Identify the blood parasite species.
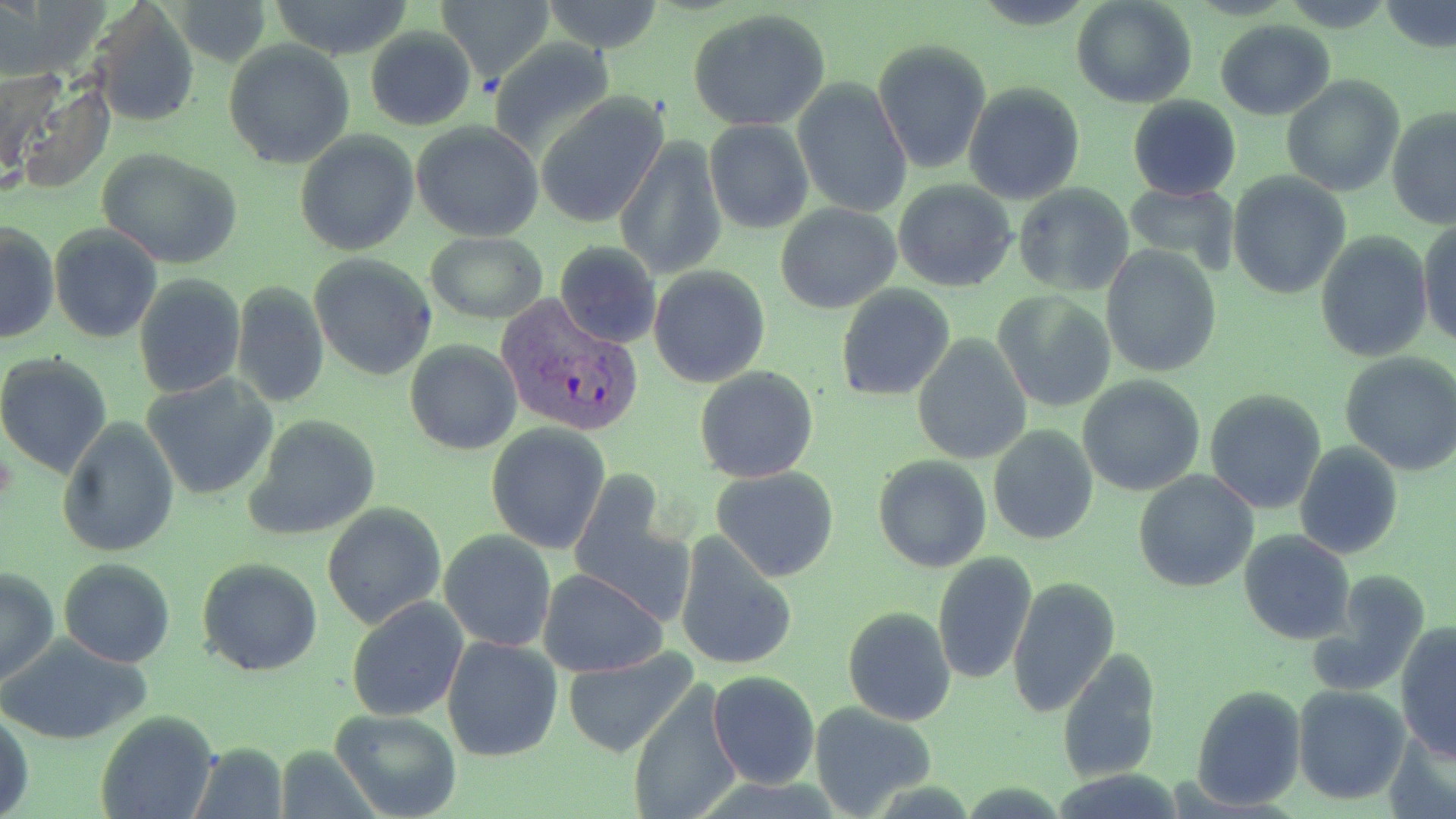
Plasmodium vivax.

Approximate bounding boxes as (x1, y1, x2, y2) in pixels. Plasmodium vivax-infected red blood cell locations: (495, 294, 646, 439). Uninfected red blood cell locations: (173, 0, 271, 67), (268, 0, 417, 61), (435, 0, 553, 82), (539, 0, 668, 53), (1072, 0, 1198, 109), (1381, 2, 1456, 53), (88, 3, 201, 128), (687, 10, 832, 132), (1215, 19, 1335, 119), (364, 28, 477, 131), (488, 38, 617, 158), (873, 40, 993, 176), (223, 41, 354, 170), (4, 69, 114, 195), (1280, 75, 1404, 198), (792, 78, 912, 218), (962, 82, 1085, 206), (537, 92, 670, 230), (1127, 94, 1242, 201), (1387, 106, 1456, 229), (704, 120, 815, 235), (411, 121, 545, 242), (294, 129, 420, 258), (615, 137, 729, 280), (96, 148, 243, 269), (1227, 173, 1350, 300), (892, 179, 1017, 293), (1013, 182, 1136, 297), (1125, 182, 1238, 273), (775, 203, 901, 315), (1417, 218, 1456, 350), (1, 219, 59, 346), (49, 224, 163, 345), (424, 232, 548, 323), (1315, 232, 1432, 363), (552, 240, 662, 350), (1099, 245, 1221, 378), (310, 254, 437, 379), (647, 266, 772, 388), (133, 274, 246, 398), (231, 282, 330, 407), (835, 284, 956, 402), (991, 291, 1116, 415), (912, 334, 1032, 465), (403, 340, 522, 456), (1339, 351, 1456, 477), (0, 354, 114, 479), (695, 366, 820, 483), (1078, 374, 1205, 497), (142, 375, 278, 501), (1204, 389, 1326, 514), (244, 415, 381, 542), (58, 419, 179, 557), (486, 424, 611, 554), (987, 425, 1098, 546), (873, 440, 1101, 557), (1293, 442, 1403, 560), (873, 455, 993, 573), (710, 466, 840, 582), (1133, 470, 1258, 592), (570, 473, 685, 610), (322, 503, 448, 630), (438, 528, 557, 653), (1238, 530, 1354, 644), (673, 533, 800, 673), (933, 551, 1038, 686), (197, 558, 323, 677), (59, 559, 175, 667), (0, 565, 58, 686), (539, 568, 668, 676), (1307, 571, 1431, 696), (1007, 577, 1120, 720), (346, 598, 468, 722), (843, 607, 956, 725), (1394, 624, 1456, 764), (0, 632, 154, 747), (441, 635, 563, 763), (559, 646, 701, 758), (1056, 651, 1163, 785), (707, 671, 820, 789), (625, 682, 743, 819), (1292, 685, 1409, 804), (1192, 686, 1305, 809), (807, 703, 938, 818), (0, 705, 33, 819), (329, 708, 461, 819), (96, 711, 218, 819), (192, 741, 288, 818). Single field of view. Light microscopy. 1000x magnification. Thin blood film. May-Grünwald-Giemsa stain. Image is 1456×819 pixels.